Classify this cell by malaria status.
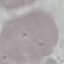
Uninfected.

capture: smartphone through the microscope eyepiece
stain: Giemsa
preparation: thin blood smear
image_type: automatically extracted cell patch, resized to 64 × 64 pixels